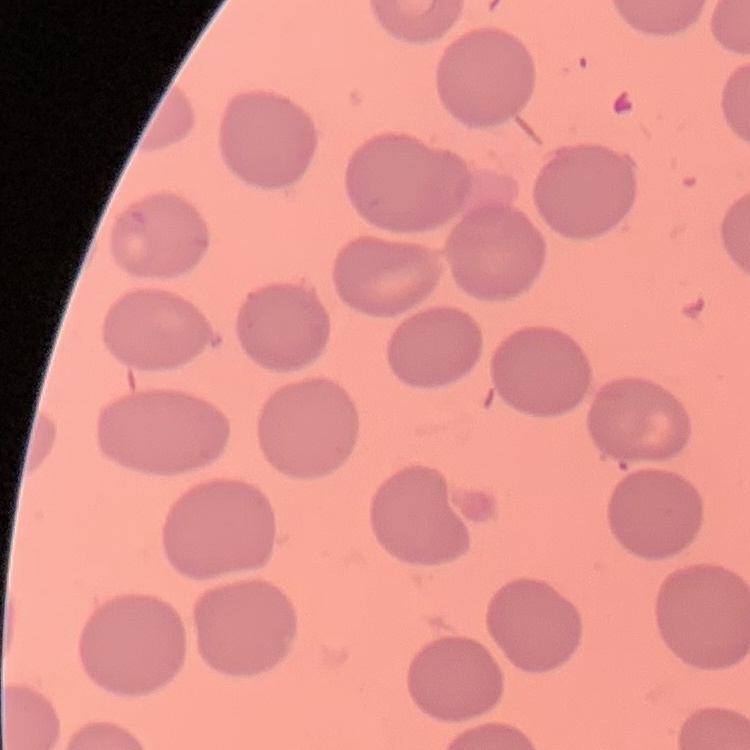
{
  "red_blood_cell_morphology": "no rouleaux formation",
  "stain": "Field's or Giemsa",
  "preparation": "thin peripheral smear",
  "image_type": "one tile cut from a larger photomicrograph"
}